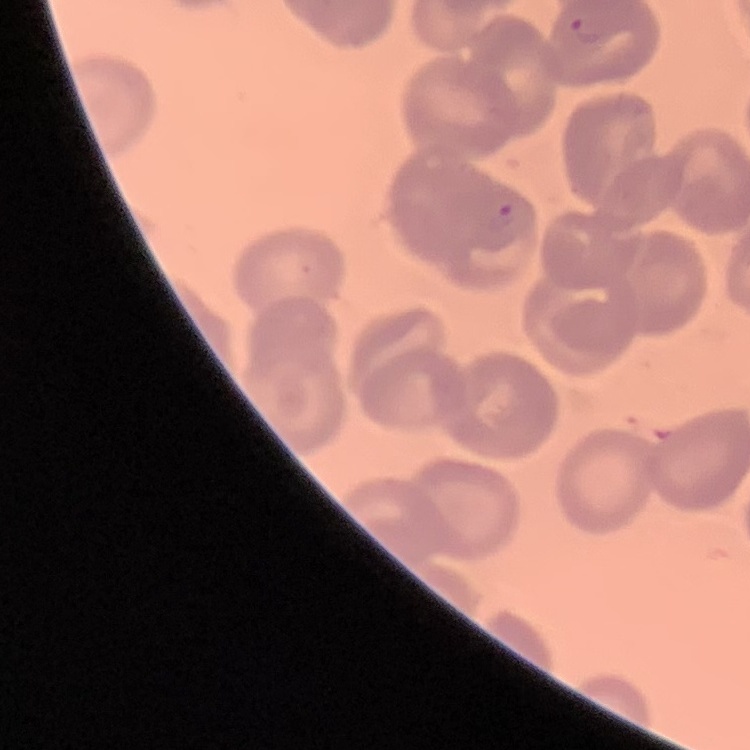
erythrocyte morphology = no rouleaux formation
stain = Field's or Giemsa
preparation = thin blood smear
image type = one tile cut from a larger photomicrograph